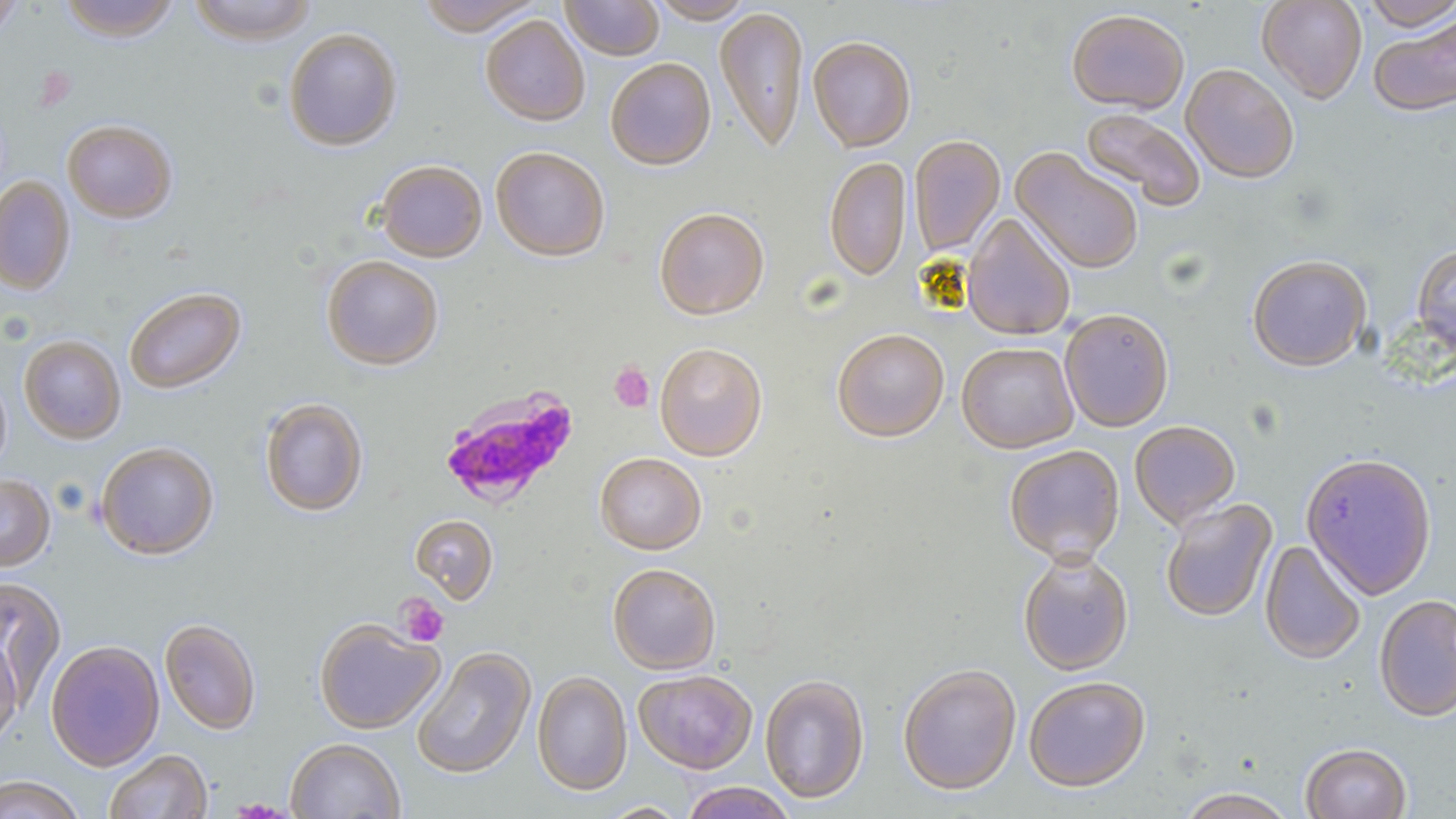

Summary:
  - Coordinate format: approximate bounding boxes as named x1/y1/x2/y2 corners in pixels
  - Platelet locations: (x1=609, y1=363, x2=655, y2=413), (x1=395, y1=593, x2=449, y2=647)
  - Plasmodium falciparum-infected red blood cell locations: (x1=438, y1=385, x2=581, y2=511)
  - Uninfected red blood cell locations: (x1=57, y1=0, x2=182, y2=41), (x1=186, y1=0, x2=319, y2=45), (x1=415, y1=0, x2=544, y2=36), (x1=560, y1=0, x2=665, y2=60), (x1=647, y1=0, x2=756, y2=23), (x1=1257, y1=0, x2=1367, y2=103), (x1=1359, y1=0, x2=1456, y2=31), (x1=0, y1=1, x2=24, y2=39), (x1=715, y1=6, x2=808, y2=153), (x1=1067, y1=9, x2=1189, y2=114), (x1=1368, y1=14, x2=1456, y2=117), (x1=480, y1=15, x2=590, y2=125), (x1=283, y1=27, x2=402, y2=151), (x1=807, y1=35, x2=916, y2=152), (x1=605, y1=57, x2=716, y2=170), (x1=1181, y1=63, x2=1299, y2=184), (x1=1080, y1=108, x2=1205, y2=211), (x1=62, y1=119, x2=177, y2=223), (x1=909, y1=135, x2=1005, y2=258), (x1=490, y1=146, x2=610, y2=261), (x1=1011, y1=148, x2=1143, y2=274), (x1=824, y1=156, x2=911, y2=282), (x1=375, y1=160, x2=487, y2=262), (x1=0, y1=176, x2=75, y2=294), (x1=654, y1=207, x2=769, y2=320), (x1=962, y1=213, x2=1076, y2=341), (x1=1412, y1=245, x2=1456, y2=359), (x1=321, y1=255, x2=443, y2=370), (x1=1247, y1=255, x2=1372, y2=372), (x1=124, y1=286, x2=245, y2=393), (x1=1059, y1=309, x2=1174, y2=432), (x1=831, y1=329, x2=950, y2=443), (x1=19, y1=335, x2=125, y2=443), (x1=655, y1=342, x2=767, y2=461), (x1=956, y1=342, x2=1078, y2=454), (x1=0, y1=370, x2=11, y2=479), (x1=259, y1=397, x2=368, y2=516), (x1=1129, y1=421, x2=1241, y2=529), (x1=96, y1=441, x2=219, y2=559), (x1=1004, y1=445, x2=1125, y2=564), (x1=595, y1=452, x2=706, y2=554), (x1=1300, y1=452, x2=1437, y2=599), (x1=0, y1=474, x2=55, y2=571), (x1=1160, y1=498, x2=1277, y2=624), (x1=410, y1=514, x2=498, y2=603), (x1=1259, y1=540, x2=1366, y2=665), (x1=1017, y1=551, x2=1133, y2=675), (x1=608, y1=563, x2=721, y2=675), (x1=0, y1=577, x2=66, y2=705), (x1=1374, y1=594, x2=1456, y2=723), (x1=160, y1=618, x2=261, y2=735), (x1=314, y1=618, x2=445, y2=734), (x1=0, y1=637, x2=23, y2=749), (x1=45, y1=639, x2=165, y2=771), (x1=412, y1=647, x2=536, y2=779), (x1=897, y1=664, x2=1022, y2=796), (x1=633, y1=669, x2=757, y2=774), (x1=532, y1=670, x2=632, y2=795), (x1=760, y1=674, x2=870, y2=804), (x1=1024, y1=677, x2=1151, y2=793), (x1=285, y1=738, x2=405, y2=818), (x1=1301, y1=743, x2=1412, y2=819), (x1=103, y1=749, x2=212, y2=819), (x1=1, y1=776, x2=86, y2=819), (x1=679, y1=782, x2=798, y2=819), (x1=1177, y1=787, x2=1297, y2=818), (x1=598, y1=802, x2=689, y2=818)
  - Slide-level diagnosis: Plasmodium falciparum
  - Magnification: 1000x
  - Modality: optical microscopy
  - Image size: 1456×819 pixels
  - Stain: May-Grünwald-Giemsa
  - Preparation: thin blood film
  - Field of view: single